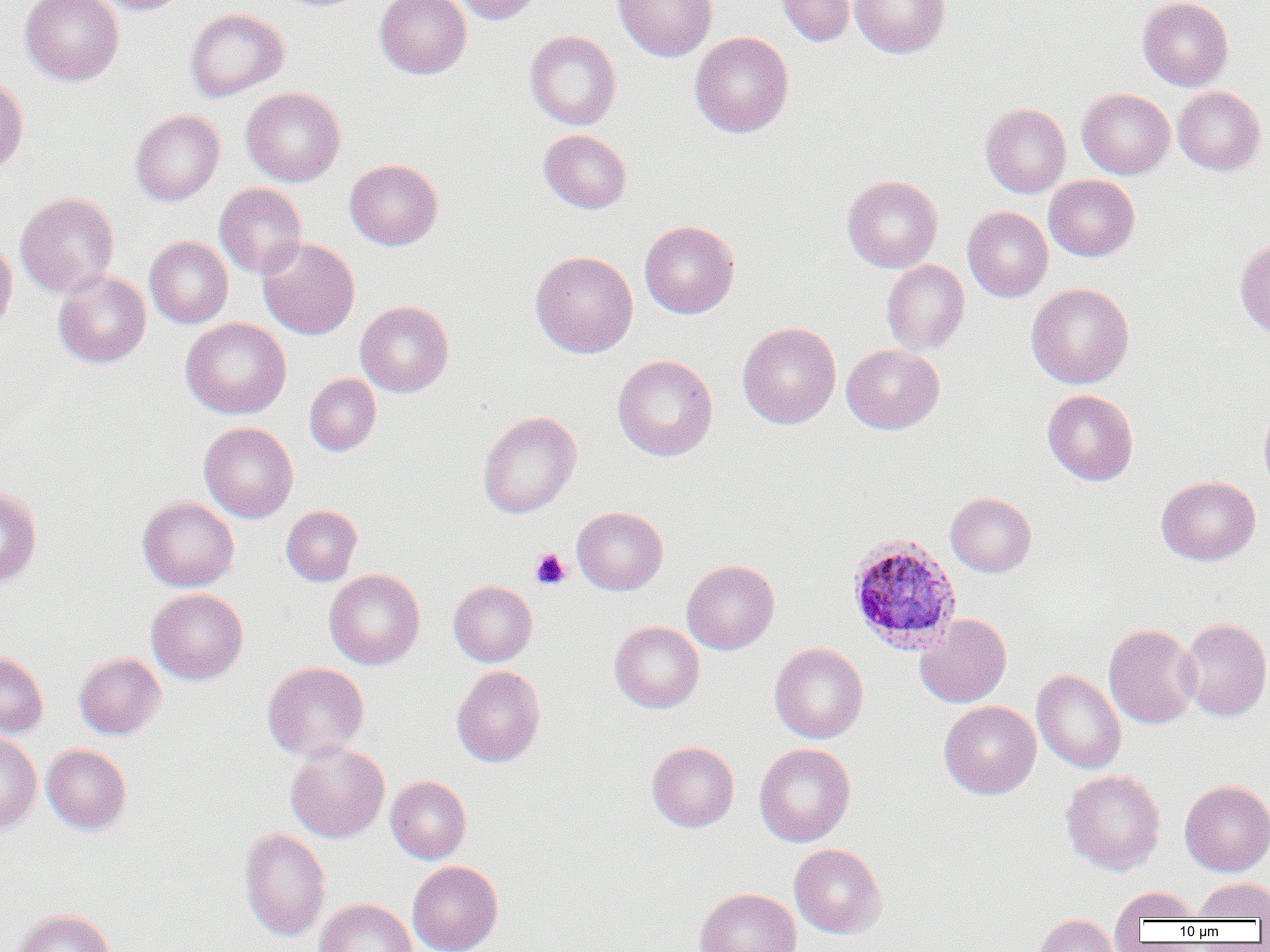

Summary:
  - Coordinate format: approximate bounding boxes as named x1/y1/x2/y2 corners in pixels
  - Uninfected red blood cell locations: (x1=20, y1=0, x2=124, y2=86), (x1=92, y1=0, x2=192, y2=15), (x1=272, y1=0, x2=372, y2=12), (x1=374, y1=0, x2=472, y2=79), (x1=454, y1=0, x2=546, y2=25), (x1=613, y1=0, x2=717, y2=62), (x1=775, y1=0, x2=856, y2=47), (x1=850, y1=0, x2=950, y2=59), (x1=1137, y1=0, x2=1233, y2=91), (x1=184, y1=8, x2=289, y2=102), (x1=524, y1=30, x2=622, y2=130), (x1=690, y1=32, x2=793, y2=138), (x1=0, y1=75, x2=29, y2=175), (x1=1172, y1=86, x2=1265, y2=176), (x1=241, y1=87, x2=345, y2=187), (x1=1077, y1=88, x2=1175, y2=179), (x1=980, y1=103, x2=1071, y2=198), (x1=130, y1=110, x2=225, y2=206), (x1=538, y1=129, x2=632, y2=214), (x1=344, y1=159, x2=443, y2=250), (x1=842, y1=174, x2=943, y2=273), (x1=1044, y1=175, x2=1140, y2=261), (x1=214, y1=183, x2=307, y2=279), (x1=15, y1=192, x2=119, y2=297), (x1=963, y1=207, x2=1053, y2=302), (x1=639, y1=220, x2=740, y2=319), (x1=145, y1=236, x2=233, y2=328), (x1=258, y1=237, x2=359, y2=340), (x1=1234, y1=238, x2=1270, y2=338), (x1=0, y1=239, x2=17, y2=332), (x1=530, y1=250, x2=638, y2=358), (x1=881, y1=259, x2=970, y2=355), (x1=53, y1=270, x2=151, y2=369), (x1=1026, y1=282, x2=1134, y2=389), (x1=355, y1=301, x2=454, y2=397), (x1=181, y1=317, x2=292, y2=419), (x1=738, y1=322, x2=841, y2=429), (x1=841, y1=344, x2=944, y2=434), (x1=612, y1=355, x2=717, y2=461), (x1=304, y1=373, x2=382, y2=457), (x1=1042, y1=389, x2=1138, y2=486), (x1=1258, y1=403, x2=1270, y2=497), (x1=478, y1=411, x2=581, y2=519), (x1=199, y1=422, x2=298, y2=523), (x1=1156, y1=475, x2=1260, y2=566), (x1=0, y1=485, x2=43, y2=589), (x1=945, y1=492, x2=1037, y2=577), (x1=137, y1=496, x2=239, y2=592), (x1=281, y1=505, x2=362, y2=586), (x1=572, y1=506, x2=668, y2=595), (x1=681, y1=559, x2=779, y2=655), (x1=324, y1=569, x2=425, y2=670), (x1=448, y1=580, x2=537, y2=666), (x1=147, y1=588, x2=248, y2=685), (x1=915, y1=614, x2=1012, y2=708), (x1=1178, y1=617, x2=1270, y2=722), (x1=609, y1=621, x2=704, y2=713), (x1=1103, y1=623, x2=1201, y2=729), (x1=769, y1=642, x2=868, y2=744), (x1=0, y1=651, x2=48, y2=738), (x1=73, y1=652, x2=166, y2=740), (x1=263, y1=662, x2=369, y2=761), (x1=451, y1=665, x2=545, y2=767), (x1=1032, y1=670, x2=1126, y2=774), (x1=939, y1=701, x2=1041, y2=800), (x1=0, y1=731, x2=42, y2=836), (x1=285, y1=741, x2=389, y2=843), (x1=647, y1=741, x2=739, y2=832), (x1=754, y1=743, x2=856, y2=847), (x1=42, y1=744, x2=132, y2=835), (x1=1061, y1=769, x2=1166, y2=875), (x1=386, y1=775, x2=471, y2=864), (x1=1179, y1=779, x2=1270, y2=876), (x1=238, y1=827, x2=331, y2=942), (x1=789, y1=843, x2=887, y2=939), (x1=407, y1=860, x2=503, y2=952), (x1=1193, y1=877, x2=1270, y2=920), (x1=1111, y1=886, x2=1201, y2=926), (x1=694, y1=887, x2=801, y2=952), (x1=315, y1=898, x2=417, y2=952), (x1=10, y1=908, x2=116, y2=952), (x1=1034, y1=913, x2=1119, y2=952)
  - Platelet locations: (x1=531, y1=548, x2=571, y2=590)
  - Plasmodium ovale-infected red blood cell locations: (x1=846, y1=533, x2=963, y2=656)
  - Slide-level diagnosis: Plasmodium ovale
  - Modality: optical microscopy
  - Image size: 1270×952 pixels
  - Field of view: single
  - Preparation: thin blood smear
  - Magnification: 1000x